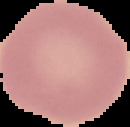 Image is 130×127 pixels. From a thin blood film. Cell region segmented out of the field of view; the surrounding area is masked to black. Malaria status: uninfected.